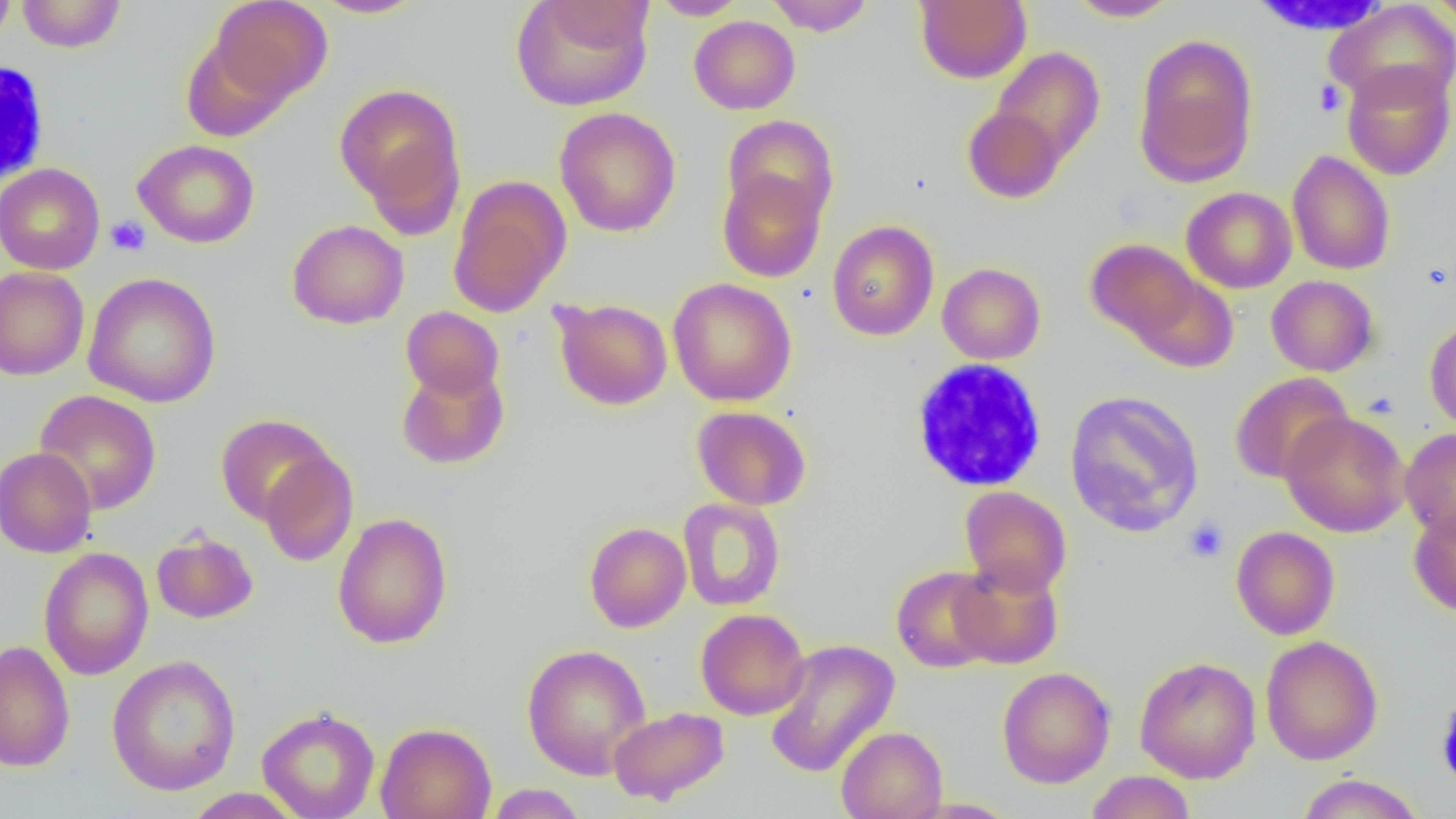
{
  "slide_level_diagnosis": "negative for blood parasites",
  "field_of_view": "one of a larger specimen",
  "uninfected_red_blood_cell_locations": "approximate bounding boxes as (x1,y1)-(x2,y2) corner pairs in pixels: (0,0)-(16,48), (17,0)-(126,53), (209,0)-(331,105), (313,0)-(425,19), (511,0)-(653,111), (650,0)-(749,20), (765,0)-(875,35), (1065,0)-(1180,21), (1427,0)-(1455,32), (914,1)-(1031,83), (1326,2)-(1456,110), (689,15)-(800,114), (181,33)-(296,140), (1133,34)-(1259,186), (990,47)-(1105,167), (1341,61)-(1455,180), (335,83)-(465,221), (962,106)-(1065,203), (555,107)-(681,237), (723,114)-(839,226), (133,139)-(260,248), (1286,150)-(1395,276), (0,163)-(105,275), (717,168)-(826,282), (449,177)-(571,317), (1181,186)-(1297,293), (287,220)-(409,329), (826,220)-(939,341), (1085,239)-(1202,343), (937,262)-(1046,364), (0,266)-(90,380), (1128,271)-(1239,374), (83,272)-(222,408), (1266,275)-(1378,376), (668,278)-(797,406), (552,298)-(672,410), (401,306)-(504,400), (1425,317)-(1456,432), (396,363)-(509,470), (1230,372)-(1353,484), (34,390)-(162,515), (1064,390)-(1205,537), (691,405)-(812,510), (1280,411)-(1411,537), (215,414)-(336,525), (1400,427)-(1456,541), (0,447)-(97,558), (259,449)-(358,566), (960,486)-(1072,596), (677,498)-(786,611), (1409,506)-(1456,617), (333,512)-(453,649), (584,522)-(691,632), (1231,526)-(1340,640), (151,528)-(258,624), (38,547)-(154,680), (951,559)-(1064,669), (891,565)-(1000,673), (695,608)-(810,720), (1260,635)-(1383,765), (764,638)-(900,778), (0,639)-(75,773), (521,643)-(651,779), (106,655)-(241,796), (1134,656)-(1261,783), (997,666)-(1115,789), (608,706)-(729,805), (257,707)-(380,819), (375,722)-(496,819), (835,726)-(947,819), (1085,770)-(1196,819), (1297,773)-(1424,818), (485,784)-(587,818), (184,788)-(304,818)",
  "magnification": "1000x",
  "platelet_locations": "approximate bounding boxes as (x1,y1)-(x2,y2) corner pairs in pixels: (1313,80)-(1346,116), (105,215)-(150,256), (1183,517)-(1229,562)",
  "preparation": "thin blood smear",
  "modality": "optical microscopy",
  "image_size": "1456×819 pixels",
  "white_blood_cell_locations": "approximate bounding boxes as (x1,y1)-(x2,y2) corner pairs in pixels: (0,58)-(49,188), (910,360)-(1047,492)"
}